Locate every Plasmodium parasite.
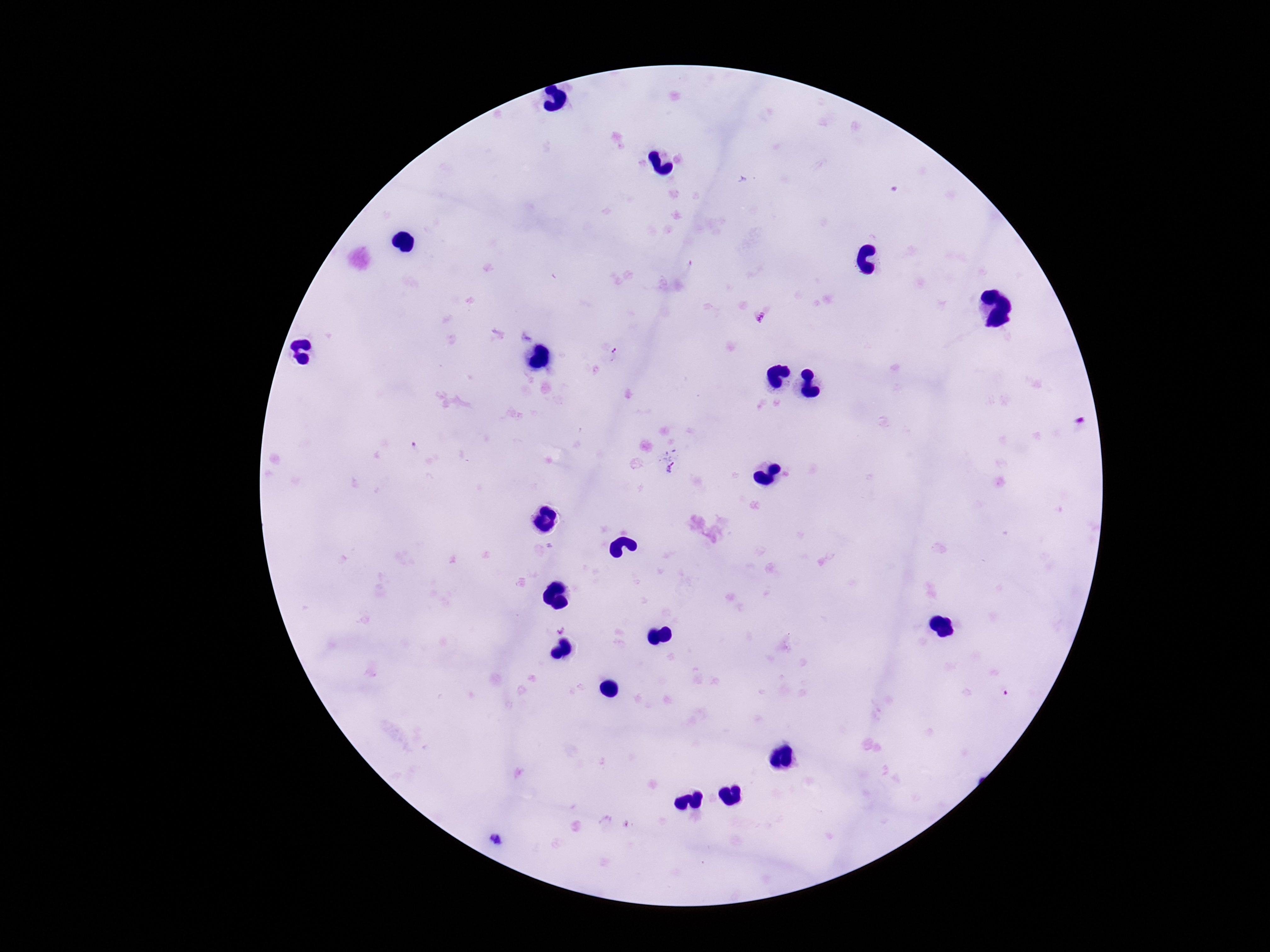

Approximate centers as {x, y} in pixels.
Plasmodium parasites: {759, 318}, {614, 355}, {1080, 420}, {670, 463}, {496, 840}.

Thick blood smear. Smartphone photograph taken through the microscope eyepiece. Giemsa-stained preparation. 100x magnification. Patient malaria status: positive. Image is 1270×952 pixels. One field from this slide.